Comment on the morphology of the red blood cells.
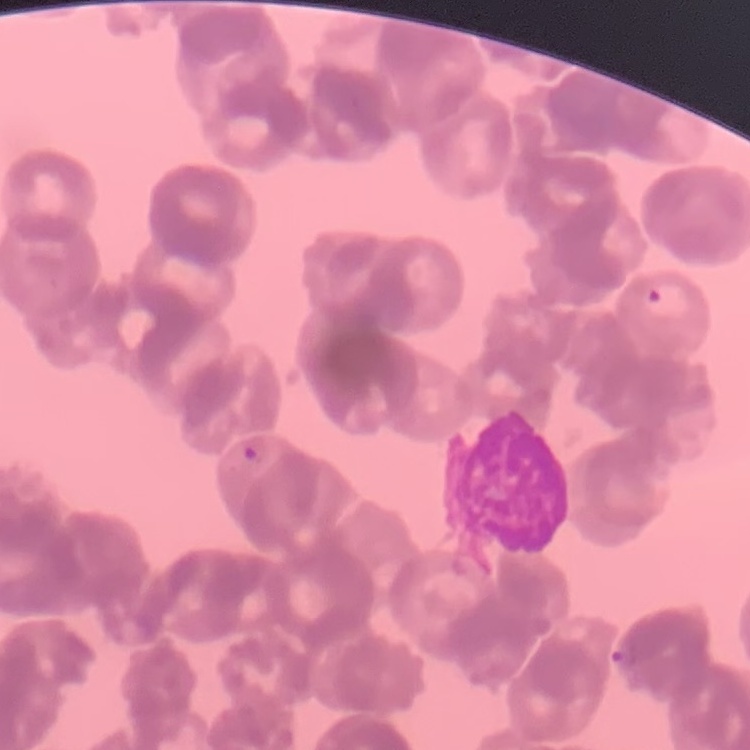

Rouleaux formation.

preparation = thin peripheral smear
stain = Field's or Giemsa
image type = one tile cut from a larger photomicrograph